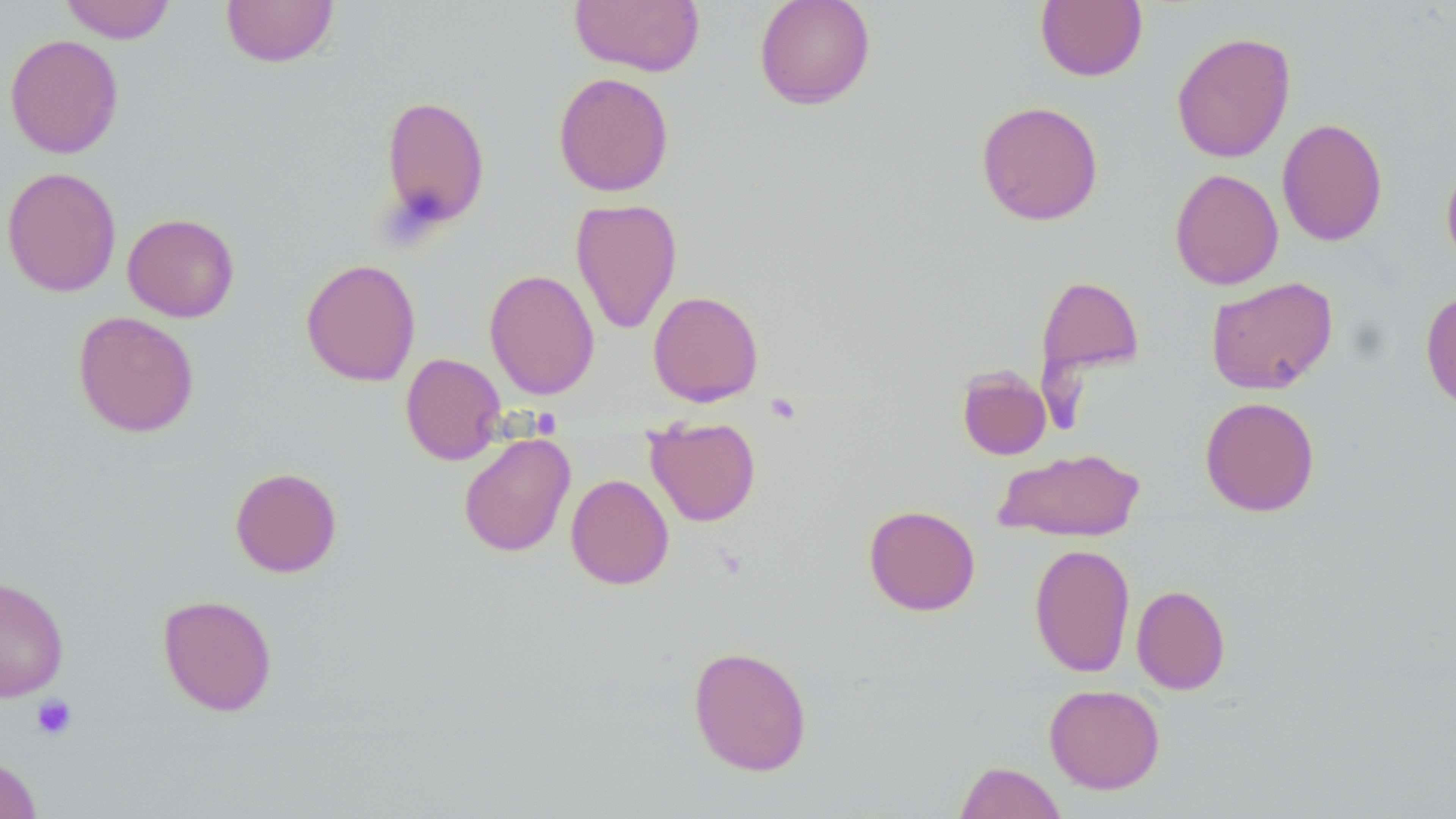

Summary:
  - Coordinate format: approximate bounding boxes as named x1/y1/x2/y2 corners in pixels
  - Platelet locations: (x1=765, y1=392, x2=802, y2=425), (x1=30, y1=694, x2=78, y2=741)
  - Uninfected red blood cell locations: (x1=60, y1=0, x2=176, y2=43), (x1=220, y1=0, x2=339, y2=67), (x1=569, y1=0, x2=705, y2=76), (x1=754, y1=0, x2=876, y2=109), (x1=1035, y1=1, x2=1148, y2=82), (x1=1171, y1=30, x2=1296, y2=163), (x1=4, y1=33, x2=124, y2=159), (x1=552, y1=71, x2=674, y2=197), (x1=379, y1=95, x2=491, y2=231), (x1=976, y1=100, x2=1104, y2=226), (x1=1277, y1=118, x2=1388, y2=247), (x1=1440, y1=156, x2=1456, y2=270), (x1=2, y1=166, x2=122, y2=297), (x1=1169, y1=168, x2=1284, y2=289), (x1=570, y1=198, x2=683, y2=335), (x1=122, y1=212, x2=240, y2=322), (x1=300, y1=258, x2=421, y2=386), (x1=484, y1=268, x2=600, y2=401), (x1=1036, y1=275, x2=1144, y2=378), (x1=1205, y1=276, x2=1338, y2=395), (x1=1420, y1=288, x2=1456, y2=414), (x1=647, y1=290, x2=764, y2=407), (x1=73, y1=311, x2=200, y2=437), (x1=401, y1=352, x2=506, y2=465), (x1=956, y1=365, x2=1052, y2=460), (x1=1200, y1=396, x2=1321, y2=517), (x1=645, y1=416, x2=761, y2=527), (x1=458, y1=431, x2=576, y2=557), (x1=994, y1=447, x2=1144, y2=542), (x1=229, y1=467, x2=342, y2=578), (x1=565, y1=473, x2=674, y2=590), (x1=864, y1=504, x2=981, y2=616), (x1=1029, y1=543, x2=1135, y2=678), (x1=0, y1=577, x2=69, y2=702), (x1=1131, y1=585, x2=1230, y2=694), (x1=157, y1=593, x2=278, y2=716), (x1=687, y1=644, x2=813, y2=776), (x1=1043, y1=684, x2=1166, y2=794), (x1=0, y1=756, x2=42, y2=819), (x1=954, y1=760, x2=1068, y2=819)
  - Slide-level diagnosis: negative for blood parasites
  - Image size: 1456×819 pixels
  - Modality: optical microscopy
  - Magnification: 1000x
  - Preparation: thin blood smear
  - Field of view: single
  - Stain: May-Grünwald-Giemsa